Locate every blood parasite and identify its species.
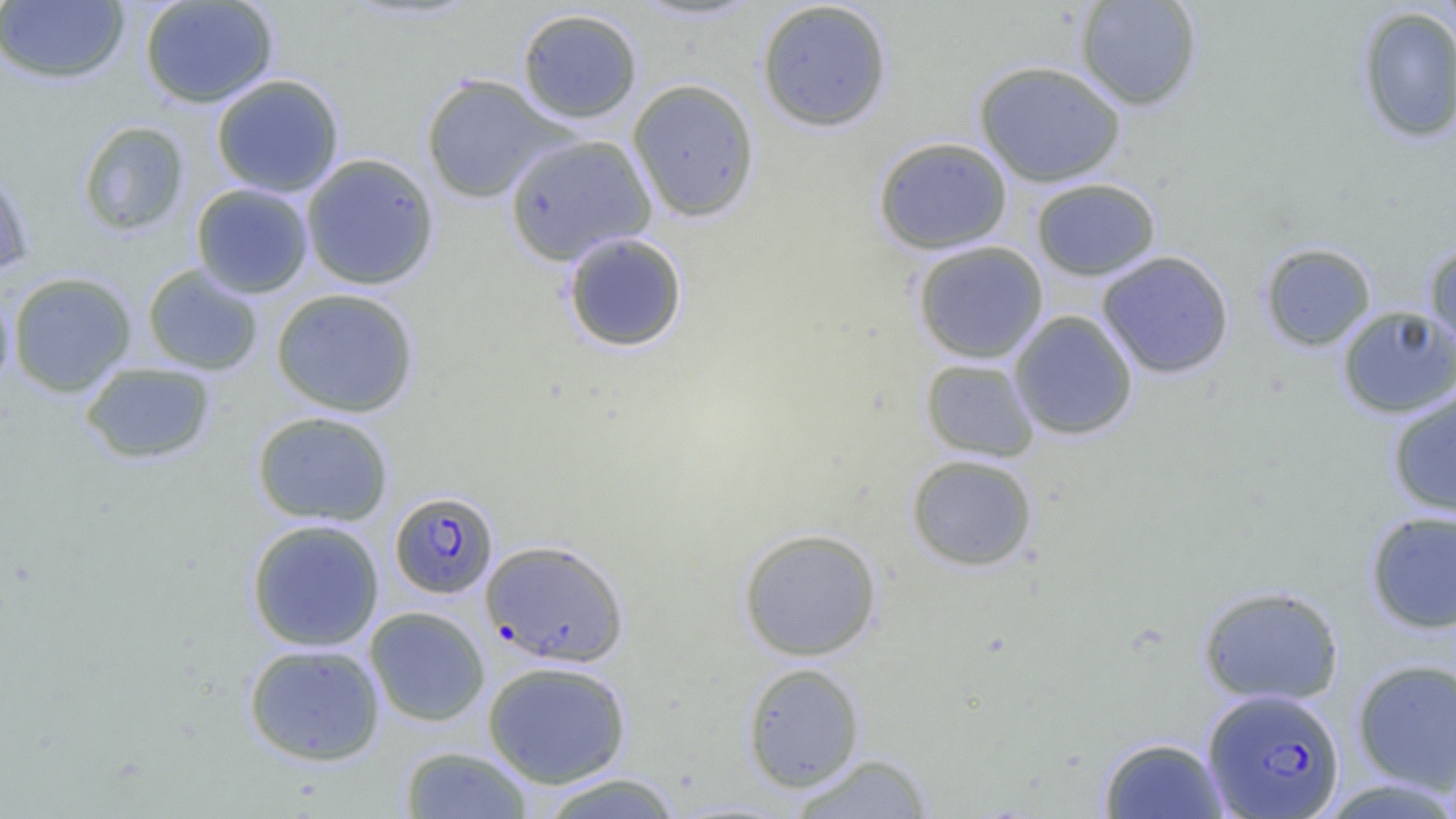
Approximate bounding boxes as [x1, y1, x2, y2] in pixels.
Plasmodium falciparum-infected red blood cells: [389, 490, 498, 599], [480, 539, 629, 667], [1202, 688, 1345, 817].
No Plasmodium ovale, Plasmodium malariae, Plasmodium vivax, Babesia divergens, or Trypanosoma brucei observed.

Uninfected red blood cell locations: [139, 0, 279, 109], [628, 0, 766, 23], [1074, 0, 1203, 111], [0, 1, 130, 85], [755, 1, 894, 133], [1356, 6, 1456, 144], [516, 7, 643, 125], [974, 60, 1127, 187], [210, 74, 345, 197], [420, 74, 568, 204], [626, 78, 761, 223], [77, 120, 190, 237], [504, 133, 656, 266], [872, 136, 1013, 255], [300, 153, 440, 290], [0, 162, 36, 277], [1030, 178, 1161, 281], [191, 184, 314, 298], [562, 231, 689, 353], [912, 241, 1049, 363], [1259, 242, 1377, 352], [1423, 242, 1456, 356], [1096, 250, 1235, 379], [142, 264, 263, 376], [7, 272, 136, 397], [0, 285, 15, 397], [270, 287, 420, 418], [1336, 305, 1456, 419], [1008, 310, 1138, 441], [919, 358, 1040, 463], [79, 361, 217, 465], [1387, 389, 1456, 519], [251, 411, 394, 527], [906, 453, 1039, 572], [1365, 510, 1456, 634], [245, 518, 385, 651], [737, 527, 883, 661], [1197, 584, 1345, 705], [364, 606, 490, 726], [243, 642, 386, 766], [1351, 658, 1456, 793], [482, 661, 632, 788], [741, 662, 866, 792], [1097, 736, 1229, 818], [399, 745, 534, 818], [788, 752, 936, 818], [536, 771, 685, 818]. Slide-level diagnosis: Plasmodium falciparum. Image is 1456×819 pixels. Optical microscopy. One field of a larger specimen. Thin blood smear. Captured at 1000x magnification.